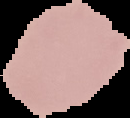
Summary:
  - Image type: segmented cell region with the area outside set to black
  - Malaria status: uninfected
  - Image size: 130×118 pixels
  - Preparation: thin blood film